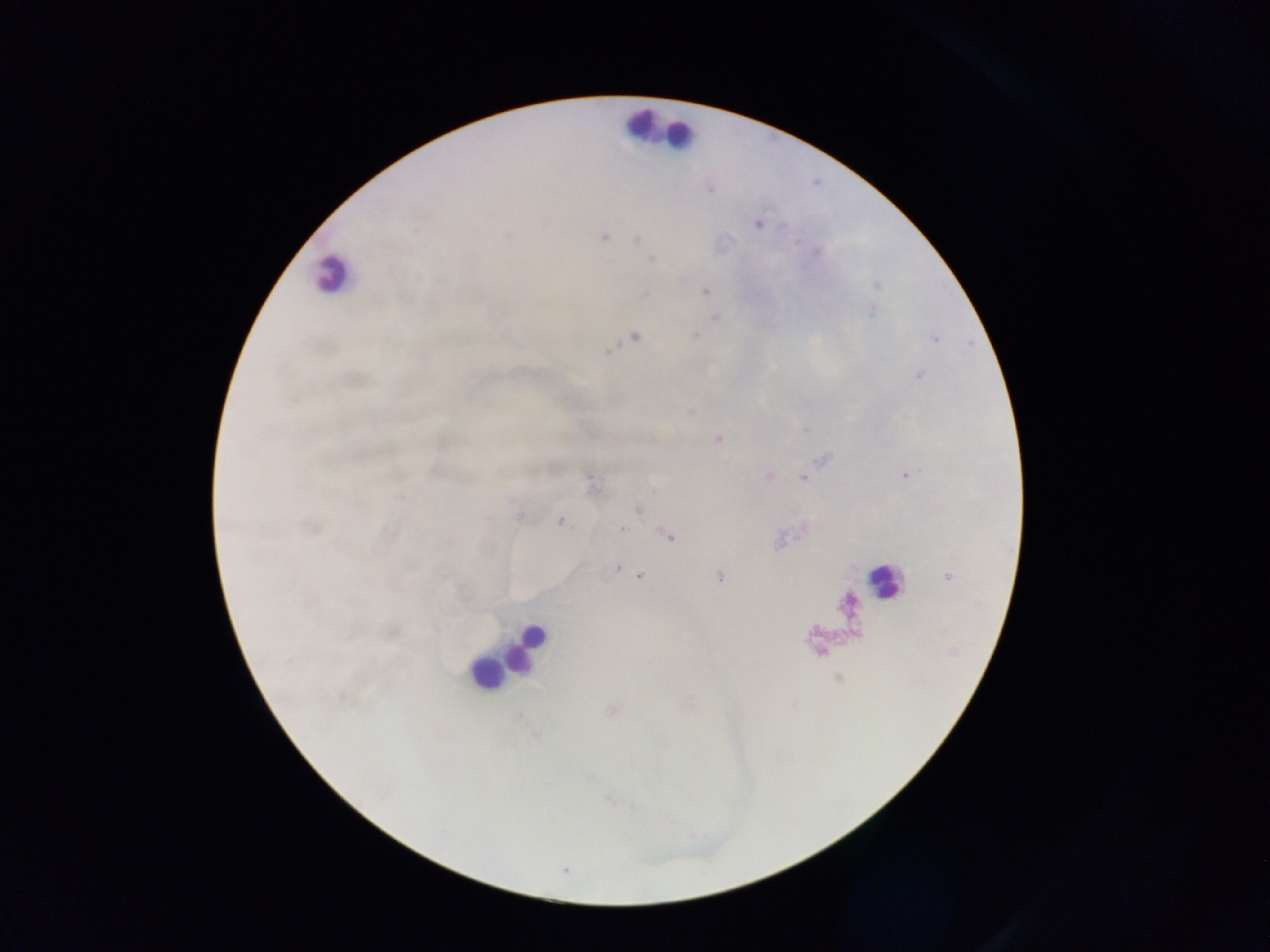 Approximate centers as (x, y) in pixels. Leukocyte locations: (639, 123), (679, 133), (330, 274), (881, 583), (525, 646), (485, 672). Malaria parasite locations: (710, 189), (757, 224), (416, 231), (604, 237), (637, 240), (652, 259), (705, 291), (645, 294), (716, 317), (695, 334), (634, 337), (718, 438), (906, 476), (803, 477), (638, 510), (520, 516), (561, 521), (621, 529), (669, 536), (617, 568), (641, 575), (947, 576), (719, 577). Image is 1270×952 pixels. Thick blood smear. One field of view. Collected in Ghana. Photographed through a microscope with a mobile-phone camera.